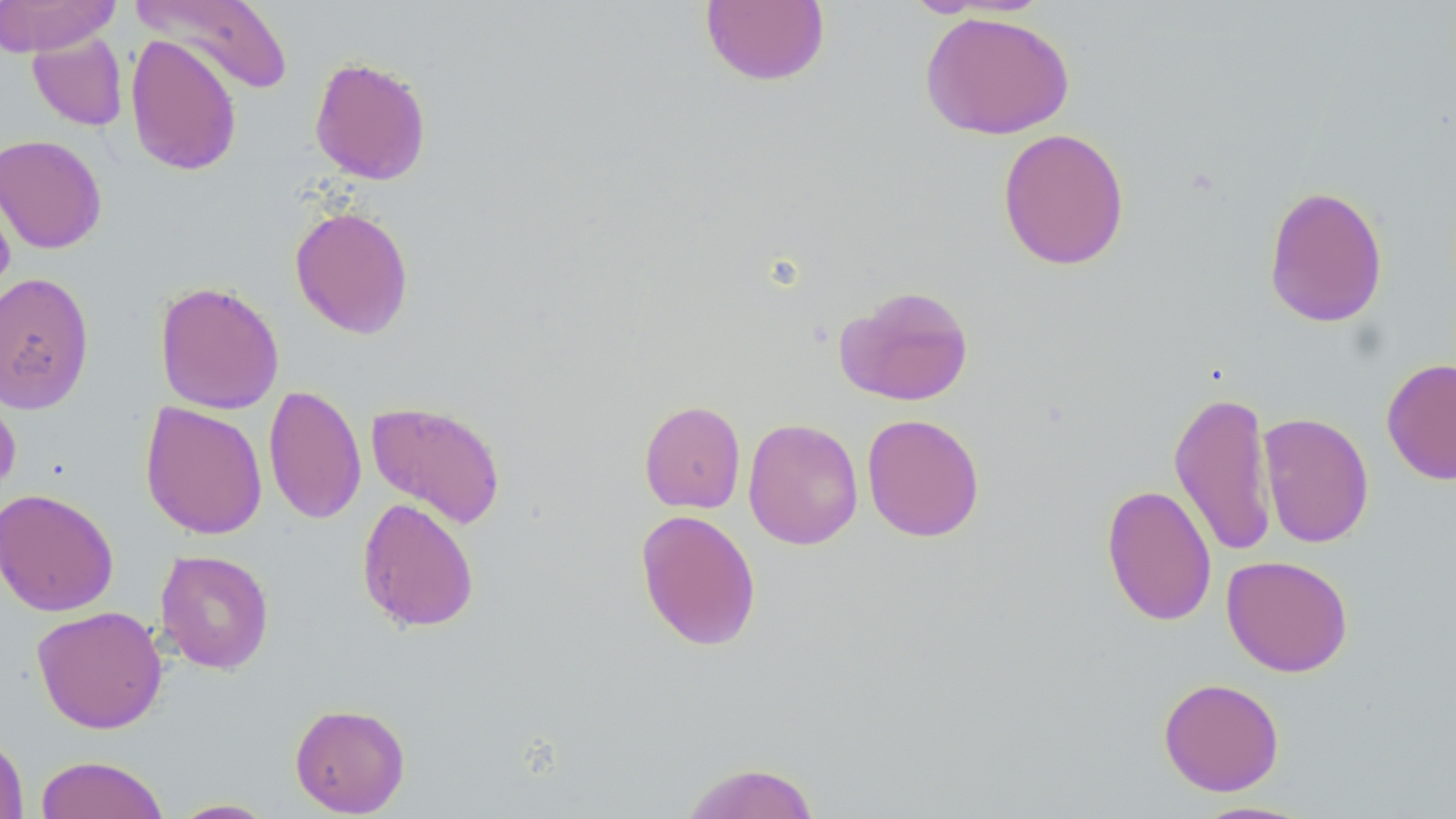

slide-level diagnosis = no evidence of blood parasites
magnification = 1000x
image size = 1456×819 pixels
stain = May-Grünwald-Giemsa
uninfected red blood cell locations = approximate bounding boxes as [x1, y1, x2, y2] in pixels: [0, 0, 122, 56], [132, 0, 293, 96], [700, 0, 830, 87], [919, 11, 1075, 140], [27, 31, 128, 132], [125, 33, 242, 177], [309, 56, 432, 185], [997, 127, 1130, 271], [0, 134, 108, 254], [0, 178, 16, 306], [1263, 184, 1388, 328], [289, 205, 414, 339], [0, 271, 95, 414], [154, 280, 285, 415], [835, 284, 975, 406], [1382, 358, 1456, 485], [0, 381, 21, 502], [263, 384, 366, 525], [1168, 389, 1277, 558], [366, 400, 507, 530], [639, 400, 746, 514], [140, 402, 268, 539], [1257, 412, 1374, 548], [861, 413, 985, 542], [743, 417, 864, 550], [1101, 483, 1217, 627], [0, 488, 119, 616], [356, 497, 480, 633], [635, 508, 762, 651], [155, 549, 275, 674], [1222, 555, 1354, 677], [31, 605, 168, 734], [1158, 677, 1285, 796], [289, 702, 410, 817], [0, 730, 29, 819], [35, 755, 170, 819], [679, 762, 821, 819], [169, 798, 279, 818], [1189, 800, 1317, 818]
modality = optical microscopy
preparation = thin blood film
field of view = single